Assess the morphology of the erythrocytes.
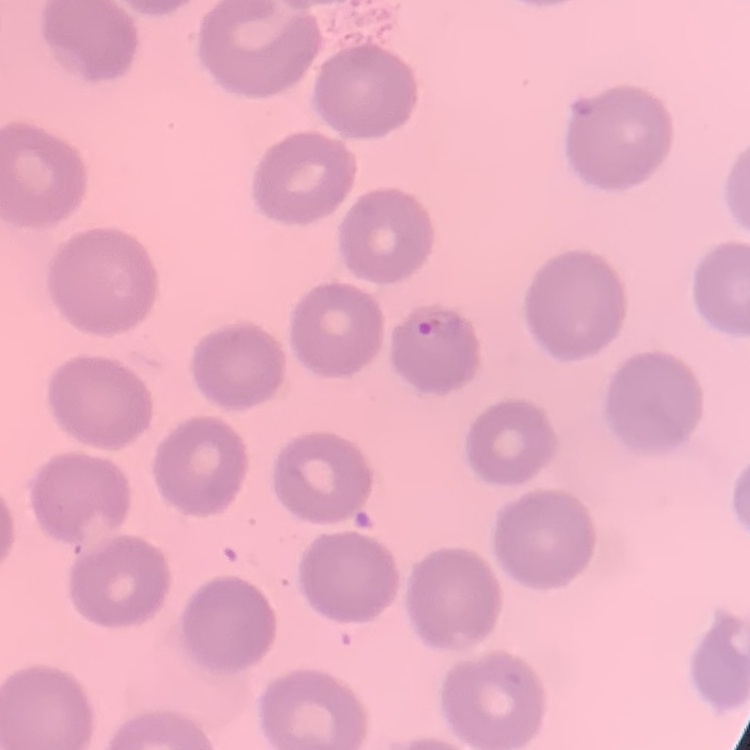

They show no rouleaux formation.

Summary:
  - Stain: Field's or Giemsa
  - Preparation: thin blood film
  - Image type: one tile cut from a larger photomicrograph